Name the cell type shown.
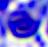

A leukocyte.

Summary:
  - Modality: photomicrograph
  - Magnification: 400x